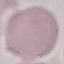

result = negative for malaria parasites
stain = Giemsa
preparation = thin blood smear
image type = cell patch, automatically extracted from a larger field of view and resized to 64 × 64 pixels
capture = smartphone camera at the microscope eyepiece